Report the malaria status.
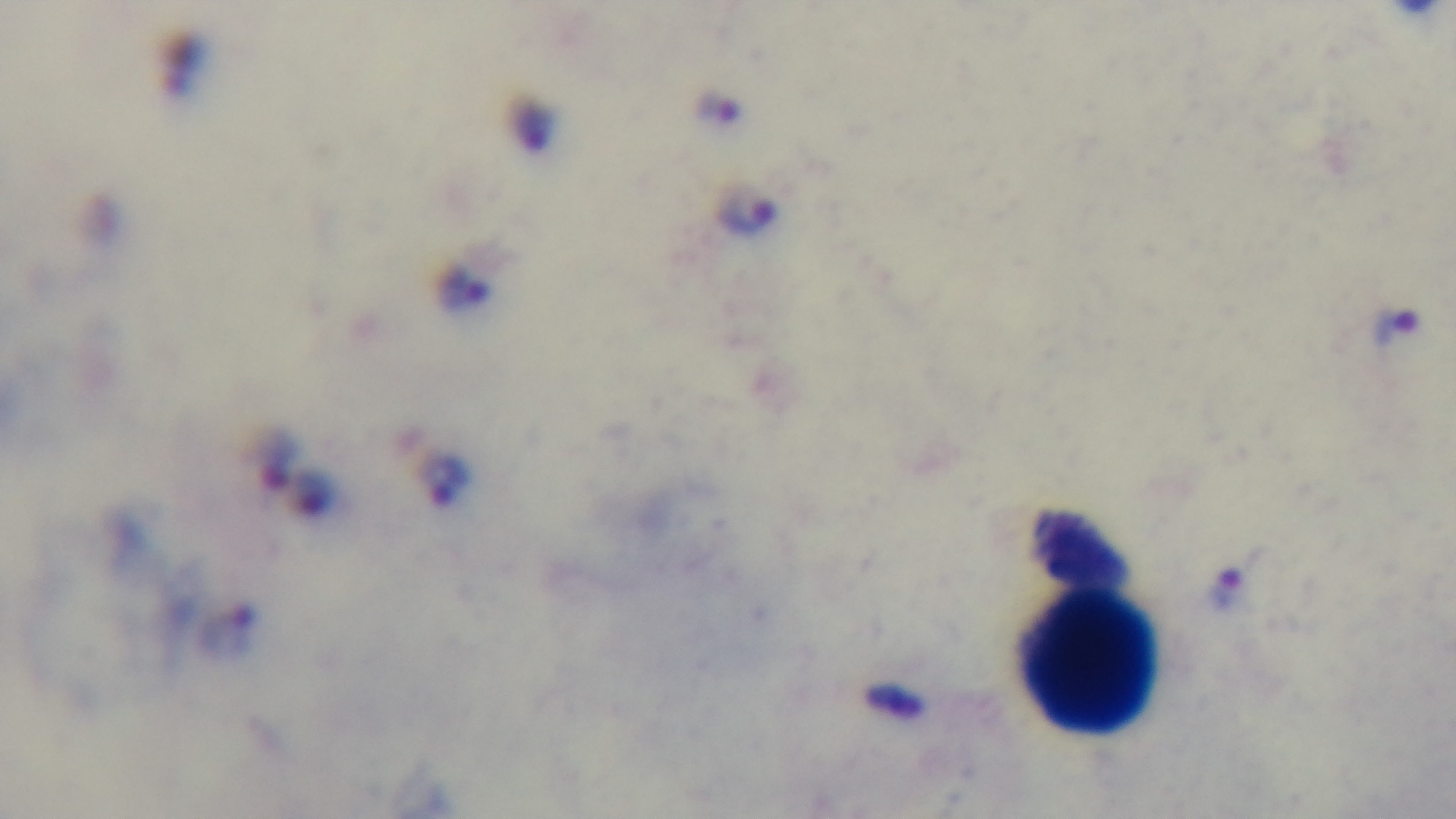

Infected.

Summary:
  - Stain: Giemsa
  - Preparation: thick smear
  - Capture: mounted 4K digital camera
  - Objective: 100x oil immersion
  - Field of view: single
  - Modality: light microscopy